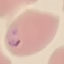
Result: malaria parasites detected. Giemsa-stained preparation. Cell patch, automatically extracted from a larger field of view and resized to 64 × 64 pixels. Photographed with a smartphone camera at the microscope eyepiece. Thin smear of blood.